Give the position of every Plasmodium parasite visible.
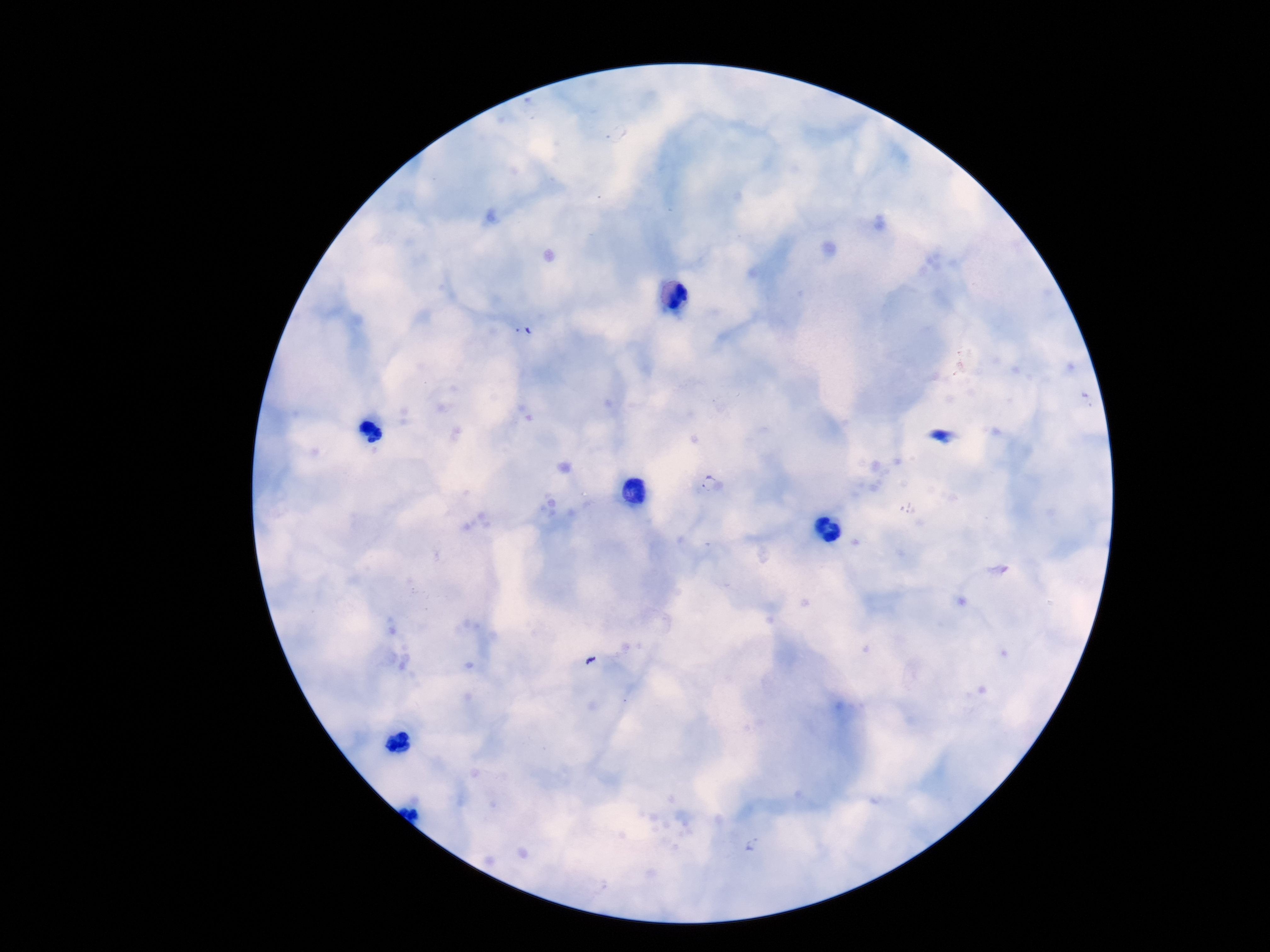
Approximate centers as (x, y) in pixels.
Plasmodium parasites: (524, 331), (711, 487), (753, 844).

magnification = 100x
stain = Giemsa
preparation = thick blood film
image size = 1270×952 pixels
field of view = single
patient malaria status = infected
capture = smartphone camera through the microscope eyepiece